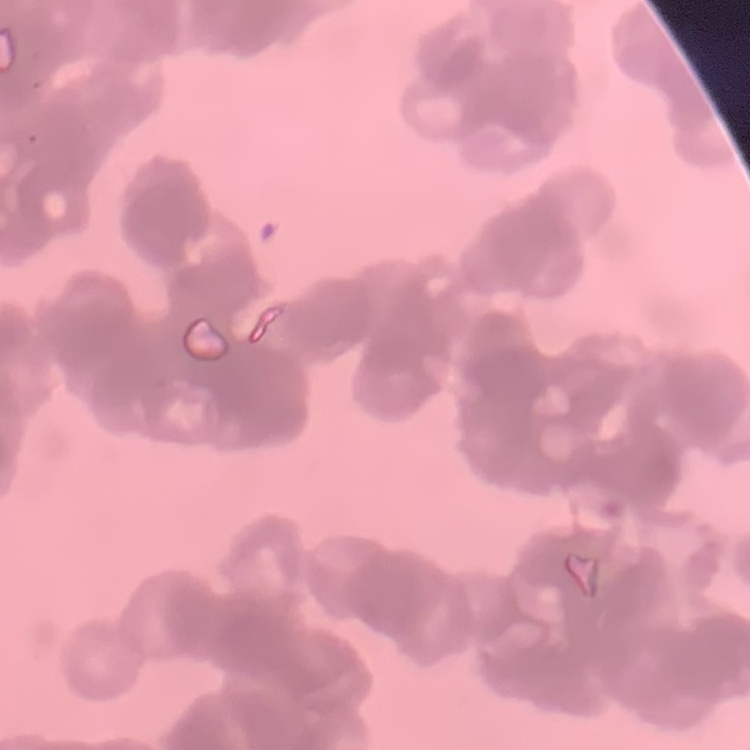

Summary:
  - Erythrocyte morphology: rouleaux formation
  - Stain: Field's or Giemsa
  - Preparation: thin peripheral smear
  - Image type: square crop of a larger photomicrograph